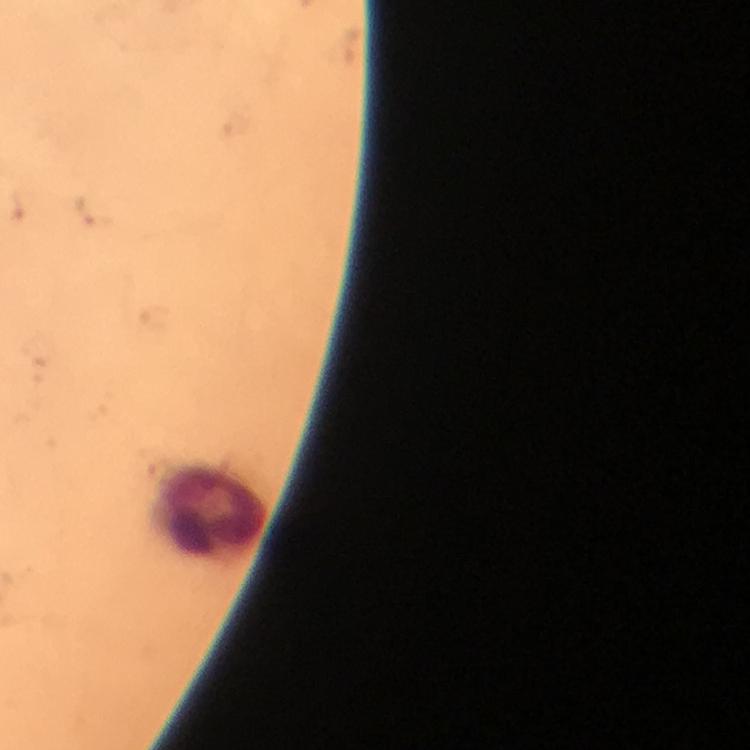
Approximate centers as {x, y} in pixels. Leukocyte locations: {208, 511}. From a diagnostic examination for malaria. A crop from one field of view. Plasmodium parasites: none seen. 100x magnification. Photographed with a smartphone mounted on the microscope. Image is 750×750 pixels. Giemsa stain. Thick smear. Immersion oil applied.